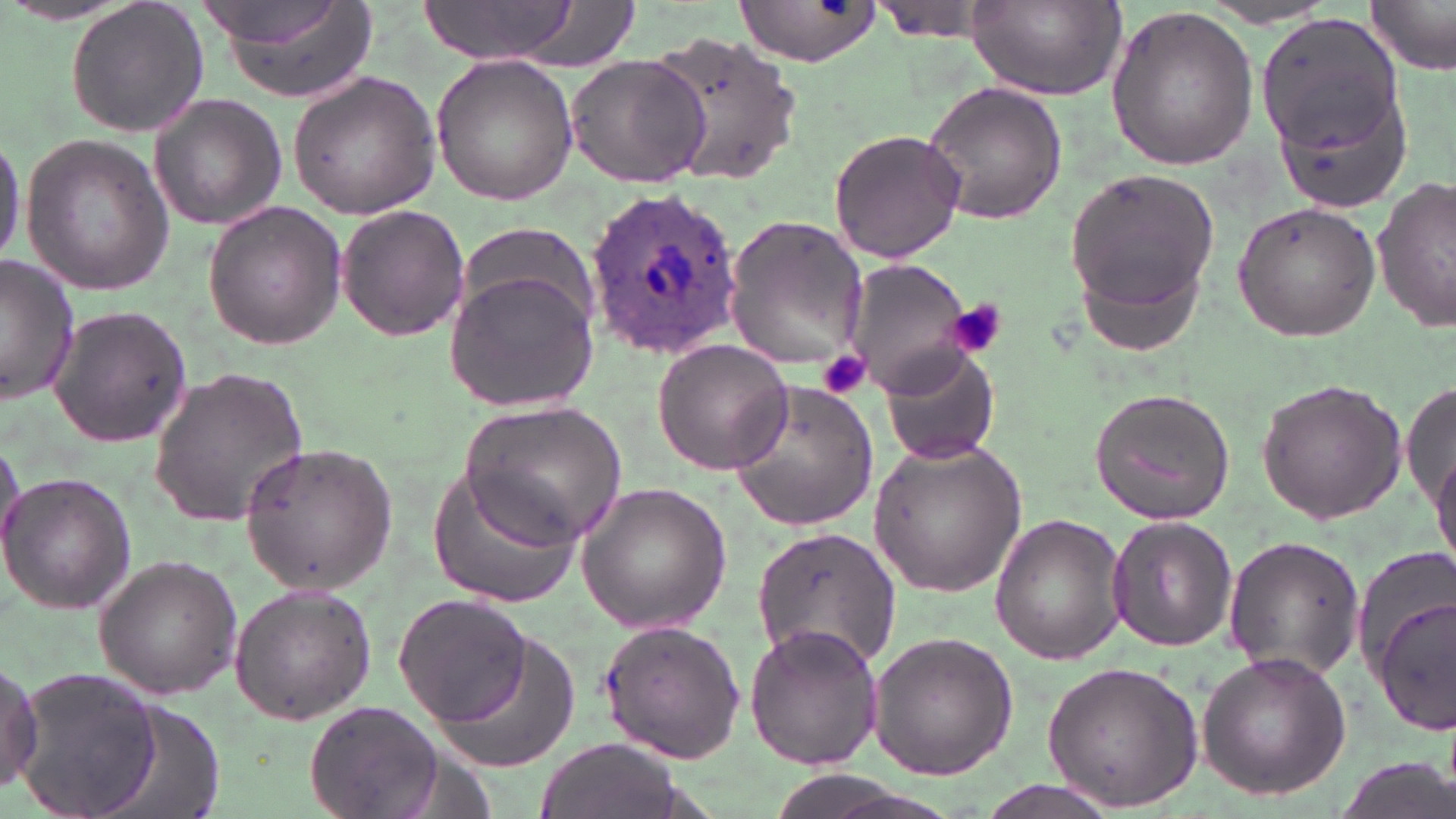
Summary:
  - Coordinate format: approximate bounding boxes as named x1/y1/x2/y2 corners in pixels
  - Plasmodium ovale-infected red blood cell locations: (x1=586, y1=187, x2=744, y2=362)
  - Uninfected red blood cell locations: (x1=65, y1=0, x2=209, y2=140), (x1=735, y1=0, x2=886, y2=65), (x1=207, y1=1, x2=380, y2=106), (x1=408, y1=1, x2=602, y2=67), (x1=969, y1=1, x2=1125, y2=101), (x1=1368, y1=1, x2=1456, y2=74), (x1=1196, y1=5, x2=1340, y2=30), (x1=1103, y1=7, x2=1260, y2=171), (x1=1252, y1=9, x2=1412, y2=175), (x1=647, y1=31, x2=805, y2=187), (x1=565, y1=53, x2=710, y2=188), (x1=430, y1=54, x2=580, y2=205), (x1=287, y1=69, x2=441, y2=221), (x1=920, y1=82, x2=1067, y2=223), (x1=148, y1=95, x2=287, y2=231), (x1=0, y1=126, x2=24, y2=272), (x1=827, y1=128, x2=967, y2=264), (x1=19, y1=136, x2=176, y2=295), (x1=1066, y1=166, x2=1222, y2=325), (x1=1372, y1=177, x2=1455, y2=332), (x1=203, y1=201, x2=347, y2=350), (x1=1231, y1=202, x2=1380, y2=341), (x1=338, y1=204, x2=469, y2=341), (x1=723, y1=216, x2=869, y2=373), (x1=0, y1=257, x2=81, y2=405), (x1=843, y1=259, x2=975, y2=394), (x1=443, y1=270, x2=598, y2=411), (x1=46, y1=305, x2=193, y2=448), (x1=651, y1=339, x2=795, y2=475), (x1=880, y1=347, x2=1000, y2=467), (x1=149, y1=364, x2=310, y2=526), (x1=1403, y1=378, x2=1456, y2=529), (x1=729, y1=380, x2=880, y2=532), (x1=1254, y1=380, x2=1408, y2=525), (x1=1087, y1=387, x2=1236, y2=525), (x1=459, y1=401, x2=626, y2=547), (x1=866, y1=435, x2=1028, y2=600), (x1=0, y1=439, x2=26, y2=566), (x1=1431, y1=439, x2=1456, y2=578), (x1=239, y1=443, x2=397, y2=594), (x1=428, y1=468, x2=582, y2=610), (x1=0, y1=471, x2=136, y2=613), (x1=574, y1=483, x2=732, y2=634), (x1=989, y1=513, x2=1130, y2=665), (x1=1106, y1=514, x2=1241, y2=651), (x1=751, y1=525, x2=900, y2=672), (x1=1223, y1=534, x2=1365, y2=685), (x1=93, y1=556, x2=243, y2=699), (x1=228, y1=581, x2=377, y2=725), (x1=1373, y1=590, x2=1456, y2=734), (x1=393, y1=591, x2=535, y2=727), (x1=421, y1=611, x2=583, y2=762), (x1=597, y1=618, x2=748, y2=762), (x1=745, y1=623, x2=885, y2=772), (x1=868, y1=632, x2=1018, y2=781), (x1=1196, y1=649, x2=1352, y2=802), (x1=0, y1=655, x2=42, y2=794), (x1=1039, y1=658, x2=1204, y2=812), (x1=15, y1=667, x2=163, y2=816), (x1=306, y1=700, x2=444, y2=819), (x1=538, y1=737, x2=680, y2=819), (x1=972, y1=783, x2=1124, y2=819)
  - Platelet locations: (x1=944, y1=300, x2=1008, y2=360), (x1=819, y1=350, x2=871, y2=400)
  - Slide-level diagnosis: Plasmodium ovale
  - Modality: optical microscopy
  - Image size: 1456×819 pixels
  - Preparation: thin blood film
  - Field of view: one of a larger specimen
  - Magnification: 1000x
  - Stain: May-Grünwald-Giemsa